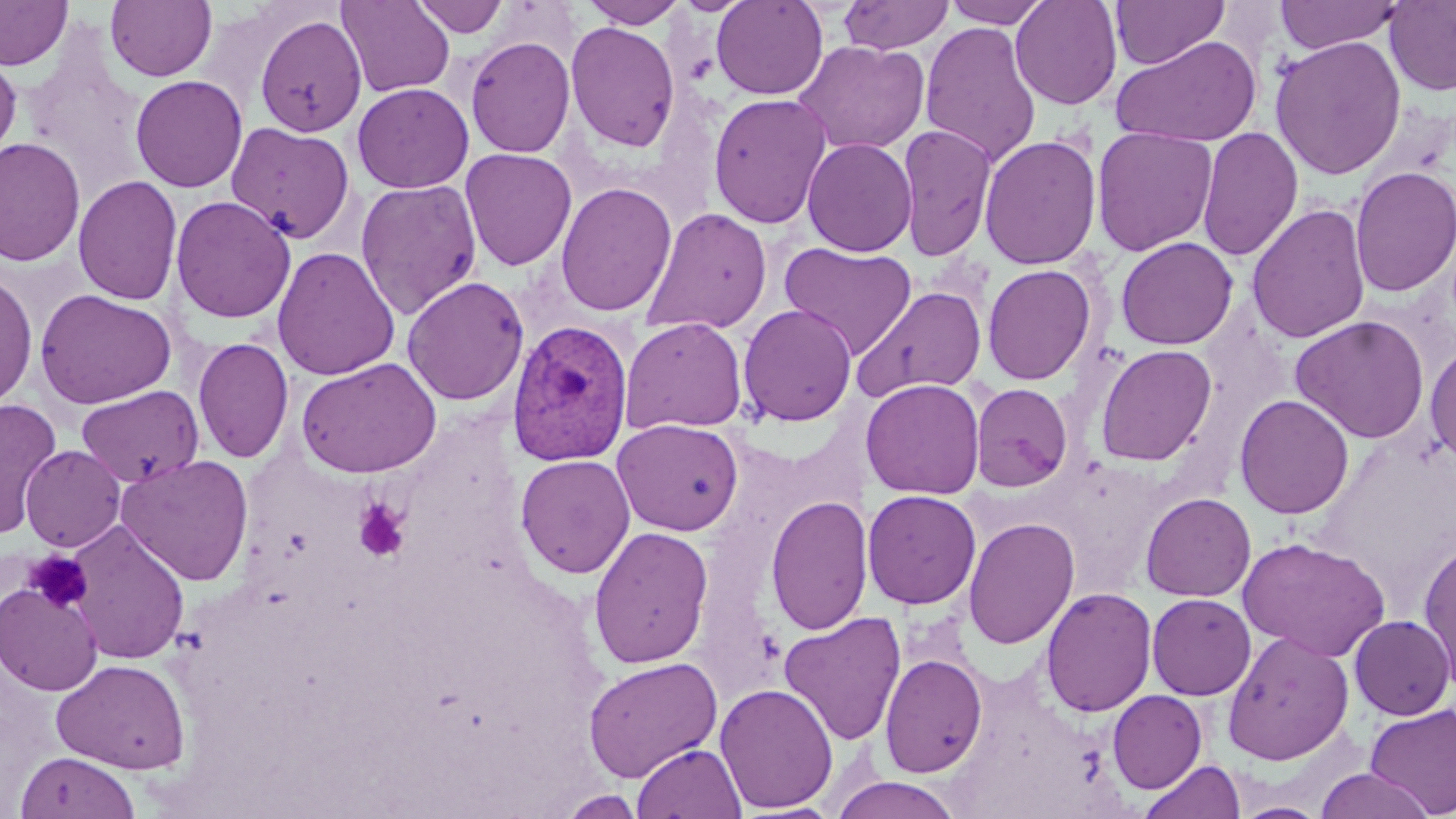
Plasmodium vivax-infected red blood cell locations = approximate bounding boxes as (x1, y1, x2, y2) in pixels: (507, 319, 635, 466)
slide-level diagnosis = Plasmodium vivax
field of view = one of a larger specimen
magnification = 1000x
stain = May-Grünwald-Giemsa
preparation = thin blood film
image size = 1456×819 pixels
uninfected red blood cell locations = approximate bounding boxes as (x1, y1, x2, y2) in pixels: (0, 0, 73, 70), (105, 0, 217, 82), (411, 0, 509, 38), (580, 0, 688, 28), (711, 0, 829, 100), (839, 0, 954, 55), (942, 0, 1051, 28), (1010, 0, 1123, 110), (1274, 0, 1405, 54), (337, 1, 455, 98), (1110, 1, 1229, 70), (1384, 1, 1456, 96), (254, 14, 367, 137), (565, 21, 681, 153), (919, 21, 1041, 168), (1110, 35, 1262, 148), (1269, 35, 1407, 180), (465, 36, 575, 158), (793, 40, 930, 155), (0, 53, 22, 166), (130, 75, 248, 193), (352, 82, 474, 194), (707, 92, 832, 229), (226, 121, 355, 244), (897, 125, 997, 261), (1091, 126, 1217, 256), (1196, 126, 1303, 262), (978, 134, 1102, 270), (0, 136, 86, 268), (802, 138, 917, 257), (459, 148, 577, 271), (1350, 165, 1456, 297), (72, 176, 183, 306), (354, 178, 482, 320), (555, 182, 677, 317), (170, 196, 296, 324), (1247, 203, 1370, 345), (641, 207, 772, 336), (1115, 237, 1238, 350), (778, 241, 918, 360), (272, 246, 399, 381), (982, 263, 1096, 385), (0, 273, 38, 409), (402, 276, 529, 405), (852, 285, 987, 401), (34, 289, 177, 409), (737, 304, 857, 427), (1290, 315, 1430, 444), (620, 316, 748, 435), (192, 337, 294, 464), (1425, 342, 1456, 470), (1095, 344, 1217, 466), (296, 357, 442, 478), (861, 378, 985, 499), (970, 383, 1073, 492), (75, 385, 203, 488), (1233, 394, 1355, 519), (1, 397, 63, 538), (611, 418, 744, 536), (20, 444, 126, 552), (116, 454, 255, 586), (515, 454, 636, 578), (862, 489, 982, 609), (1140, 492, 1256, 601), (765, 495, 872, 636), (962, 516, 1080, 650), (65, 522, 190, 665), (588, 525, 714, 669), (1237, 536, 1390, 661), (1418, 538, 1456, 694), (1, 581, 104, 696), (1040, 586, 1157, 717), (1146, 593, 1256, 700), (779, 611, 906, 746), (1349, 615, 1454, 720), (1222, 631, 1354, 765), (879, 652, 988, 778), (583, 657, 723, 781), (52, 659, 190, 774), (715, 682, 838, 813), (1107, 689, 1207, 793), (1365, 703, 1455, 817), (632, 743, 746, 818), (14, 750, 140, 819), (1139, 759, 1246, 819), (1314, 768, 1436, 819), (830, 775, 964, 818), (556, 790, 647, 818), (1232, 801, 1330, 819)
platelet locations = approximate bounding boxes as (x1, y1, x2, y2) in pixels: (353, 499, 411, 562), (23, 550, 93, 613)
modality = optical microscopy